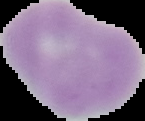

Summary:
  - Image size: 145×121 pixels
  - Image type: cell region segmented out of the field of view; surrounding area masked to black
  - Preparation: thin blood smear
  - Malaria status: uninfected